Classify this cell by malaria status.
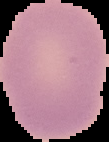

Uninfected.

image type = segmented cell region on a black background
image size = 109×142 pixels
preparation = thin blood smear